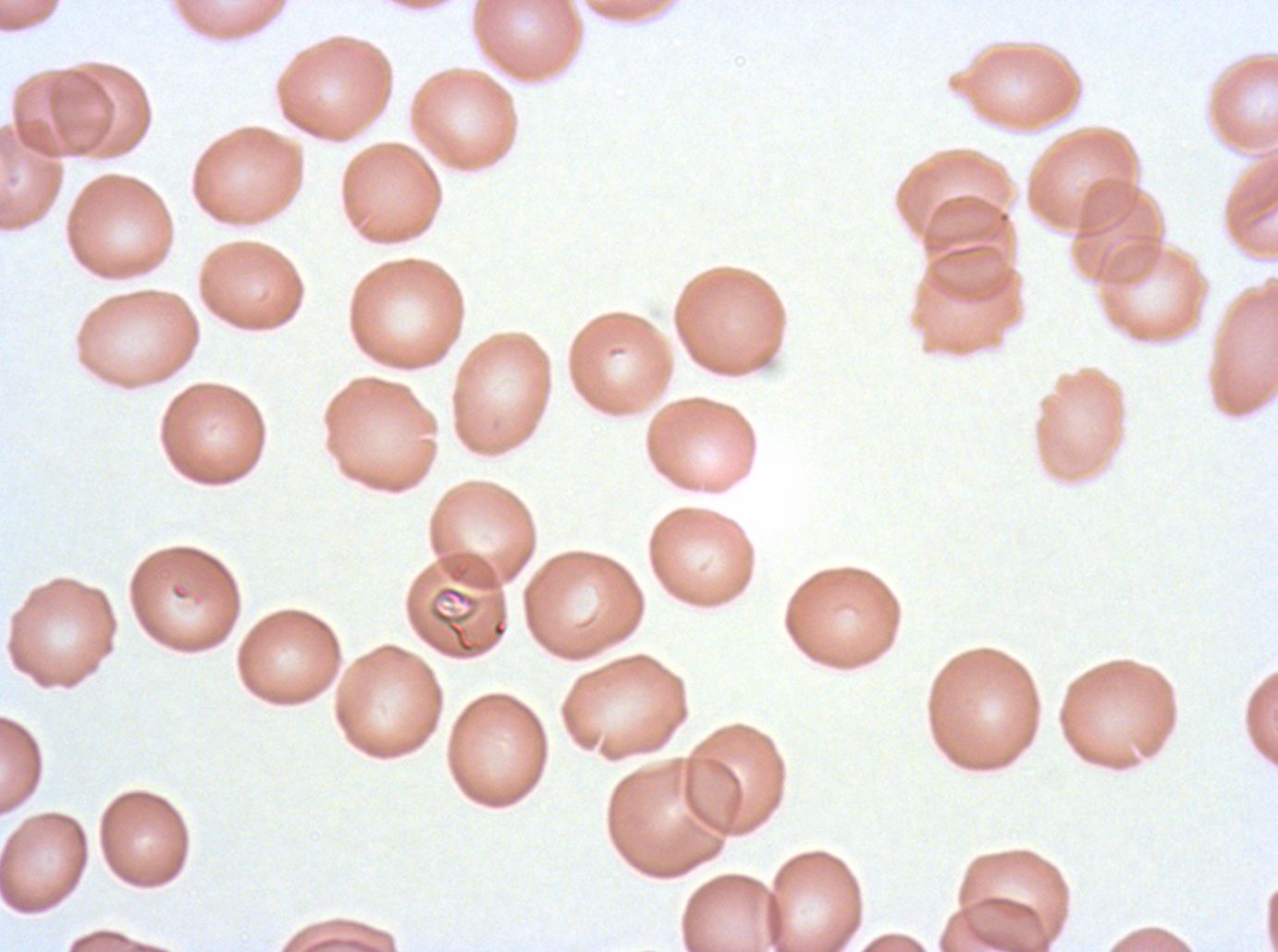
Approximate bounding boxes as [x1, y1, x2, y2] in pixels.
Summary:
  - Debris locations: [431, 605, 485, 655]
  - Field of view: one sub-image of a larger composite
  - Stain: Giemsa
  - Preparation: thin blood film
  - Image size: 1278×952 pixels
  - Specimen: P. falciparum cultured ex vivo for 24 to 48 hours, from a patient in The Gambia